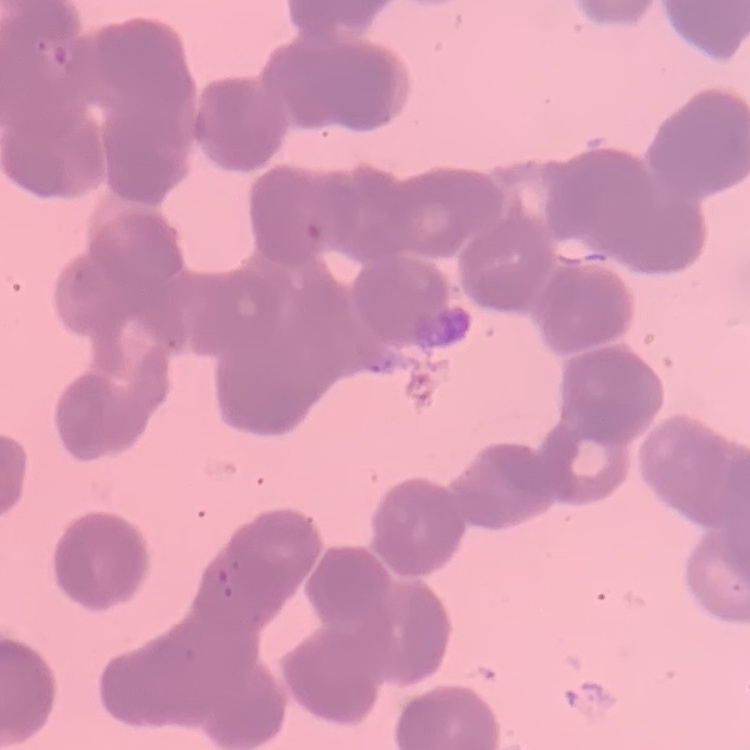
Summary:
  - Red blood cell morphology: rouleaux formation
  - Preparation: thin peripheral smear
  - Image type: square crop of a larger photomicrograph
  - Stain: Field's or Giemsa